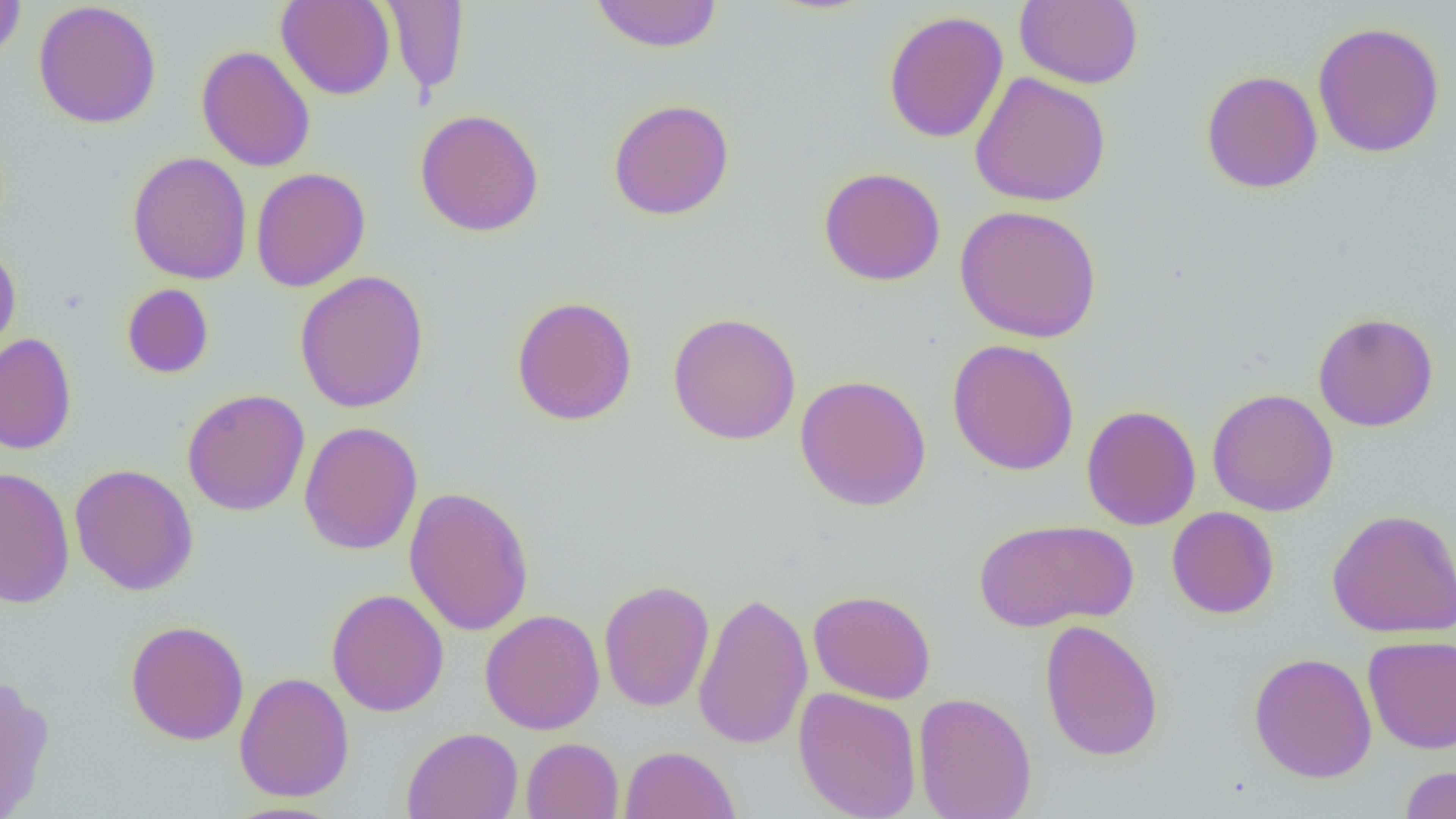

{
  "slide_level_diagnosis": "negative for blood parasites",
  "field_of_view": "single",
  "uninfected_red_blood_cell_locations": "approximate bounding boxes as (x1,y1)-(x2,y2) corner pairs in pixels: (0,0)-(27,63), (276,0)-(395,100), (589,0)-(722,53), (1014,0)-(1143,89), (33,1)-(162,129), (381,1)-(470,97), (883,10)-(1009,143), (1312,21)-(1446,158), (196,45)-(316,172), (1201,69)-(1322,194), (970,72)-(1111,207), (607,98)-(735,221), (414,108)-(544,237), (128,151)-(252,285), (818,166)-(946,286), (250,167)-(371,292), (955,204)-(1103,343), (0,243)-(21,364), (294,270)-(429,413), (121,283)-(214,379), (511,295)-(638,426), (1313,311)-(1439,432), (667,312)-(802,445), (0,333)-(77,455), (947,339)-(1080,476), (794,374)-(932,511), (1207,388)-(1339,517), (181,389)-(311,516), (1081,404)-(1201,531), (299,421)-(423,555), (69,463)-(198,596), (0,466)-(75,610), (404,486)-(535,636), (1166,506)-(1280,619), (1326,508)-(1456,638), (972,518)-(1137,632), (598,579)-(715,712), (327,589)-(449,717), (692,590)-(813,750), (808,590)-(937,704), (480,609)-(605,735), (1039,619)-(1164,761), (124,620)-(250,745), (1362,634)-(1456,754), (1248,651)-(1378,784), (234,671)-(354,802), (0,674)-(55,818), (794,687)-(923,819), (913,691)-(1036,819), (401,727)-(523,819), (521,737)-(624,819), (619,745)-(741,819), (1398,765)-(1456,819), (217,801)-(348,819)",
  "modality": "light microscopy",
  "image_size": "1456×819 pixels",
  "preparation": "thin blood film",
  "magnification": "1000x"
}